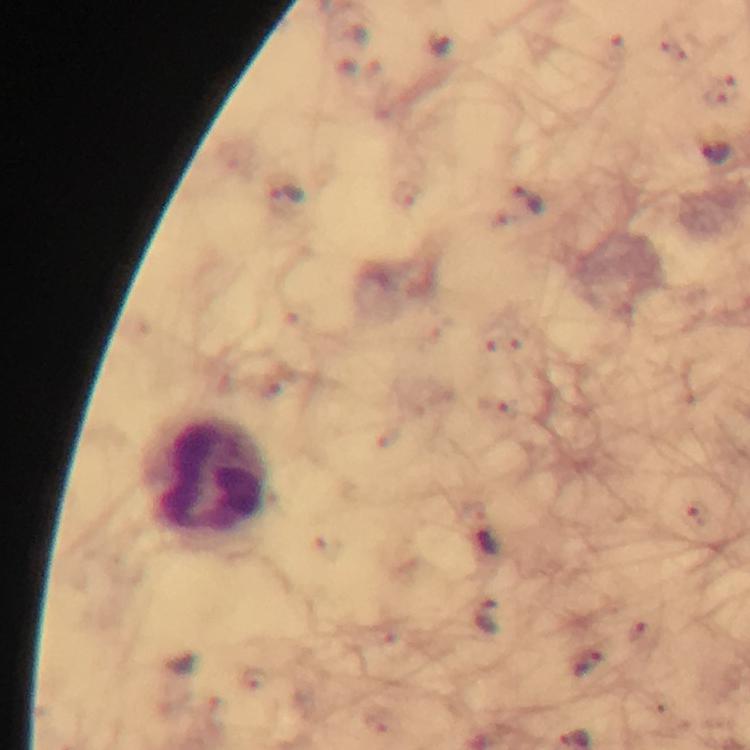
context = from a diagnostic examination for malaria
preparation = thick smear
leukocyte locations = approximate centers as {x, y} in pixels: {205, 475}
capture = smartphone camera through the microscope
stain = Giemsa
magnification = 100x
image size = 750×750 pixels
malaria parasite locations = approximate centers as {x, y} in pixels: {439, 44}, {714, 153}, {287, 194}, {528, 199}, {488, 544}, {486, 617}, {592, 665}
cropped from = one field of view
immersion oil = applied